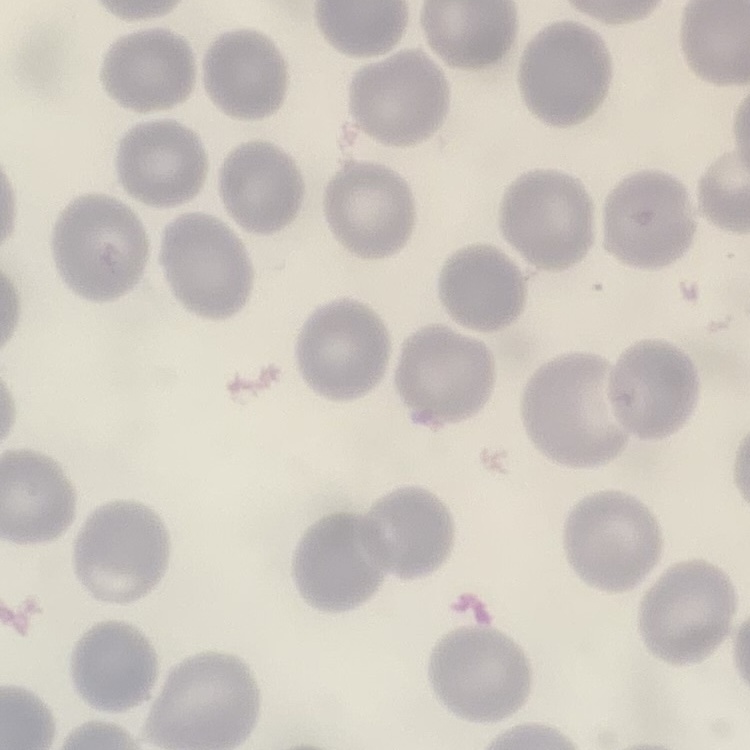
erythrocyte morphology = no rouleaux formation
image type = one tile cut from a larger photomicrograph
stain = Field's or Giemsa
preparation = thin peripheral smear